Give the extent of all uninfected red blood cells.
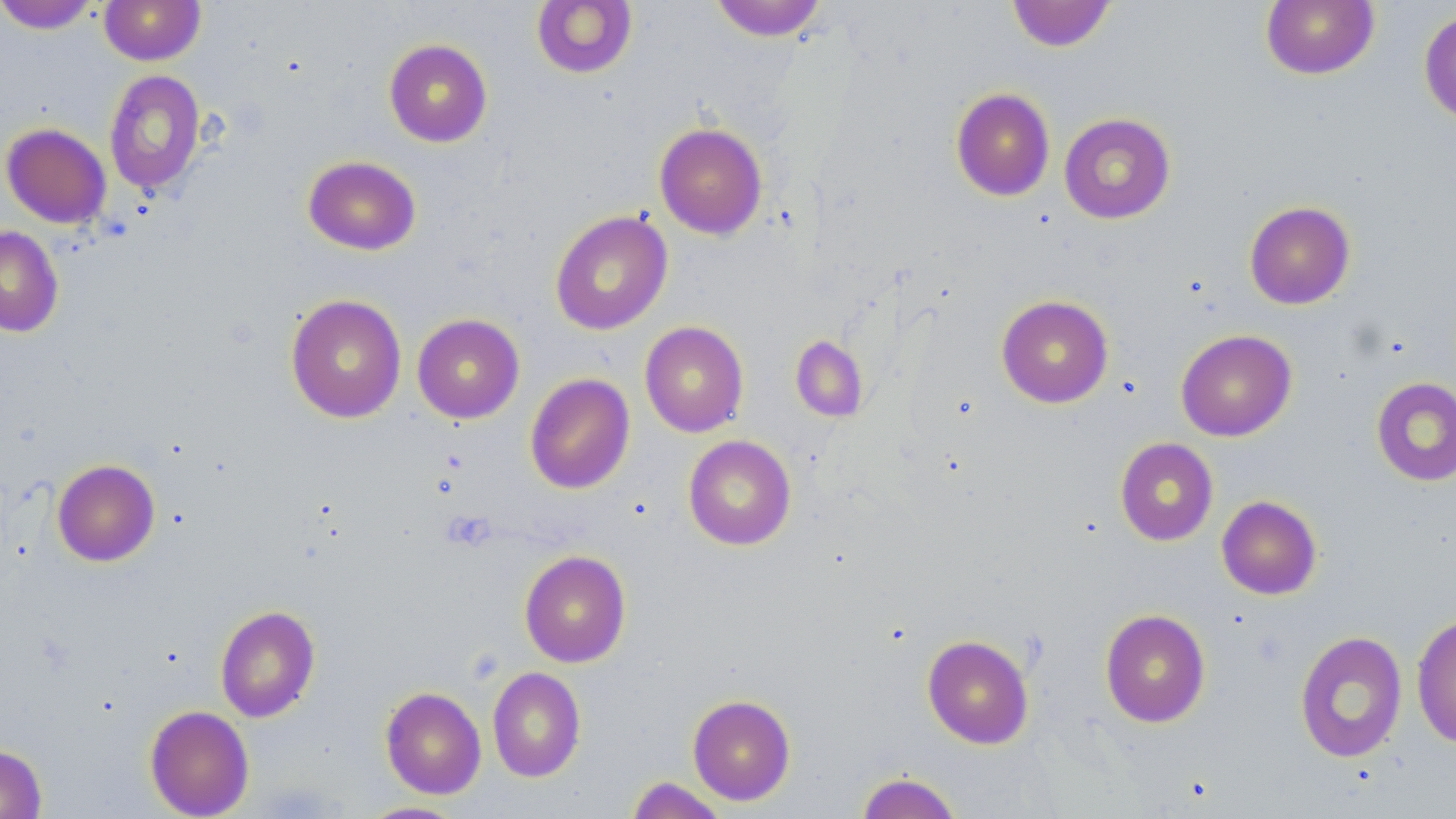

Approximate bounding boxes as [x1, y1, x2, y2] in pixels.
Uninfected red blood cells: [99, 0, 206, 65], [709, 0, 828, 41], [0, 1, 101, 34], [531, 1, 638, 79], [1006, 1, 1117, 52], [1260, 1, 1380, 80], [1418, 7, 1456, 127], [383, 39, 493, 147], [104, 70, 205, 195], [951, 87, 1055, 201], [1059, 113, 1176, 224], [654, 122, 767, 240], [1, 123, 111, 229], [302, 155, 421, 255], [1244, 201, 1356, 309], [550, 210, 673, 335], [0, 226, 64, 338], [285, 294, 407, 423], [996, 294, 1113, 408], [412, 314, 525, 423], [640, 321, 749, 437], [1175, 329, 1296, 441], [790, 335, 869, 422], [524, 373, 635, 494], [1371, 376, 1456, 487], [683, 435, 796, 550], [1115, 437, 1219, 546], [52, 459, 160, 566], [1217, 495, 1322, 599], [519, 549, 632, 668], [215, 604, 321, 722], [1099, 608, 1211, 727], [1411, 613, 1456, 749], [1294, 630, 1408, 762], [922, 634, 1034, 749], [487, 666, 585, 782], [380, 686, 486, 799], [687, 694, 796, 805], [144, 705, 254, 818], [0, 744, 47, 819], [855, 772, 963, 819], [625, 776, 729, 819], [357, 801, 467, 818].

slide-level diagnosis = negative for blood parasites
platelet locations = approximate bounding boxes as [x1, y1, x2, y2] in pixels: [441, 510, 496, 552]
field of view = one of a larger specimen
preparation = thin blood film
stain = May-Grünwald-Giemsa
image size = 1456×819 pixels
modality = light microscopy
magnification = 1000x